Identify the parasite.
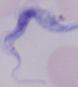
A trypanosome.

Summary:
  - Magnification: 1000x
  - Modality: micrograph